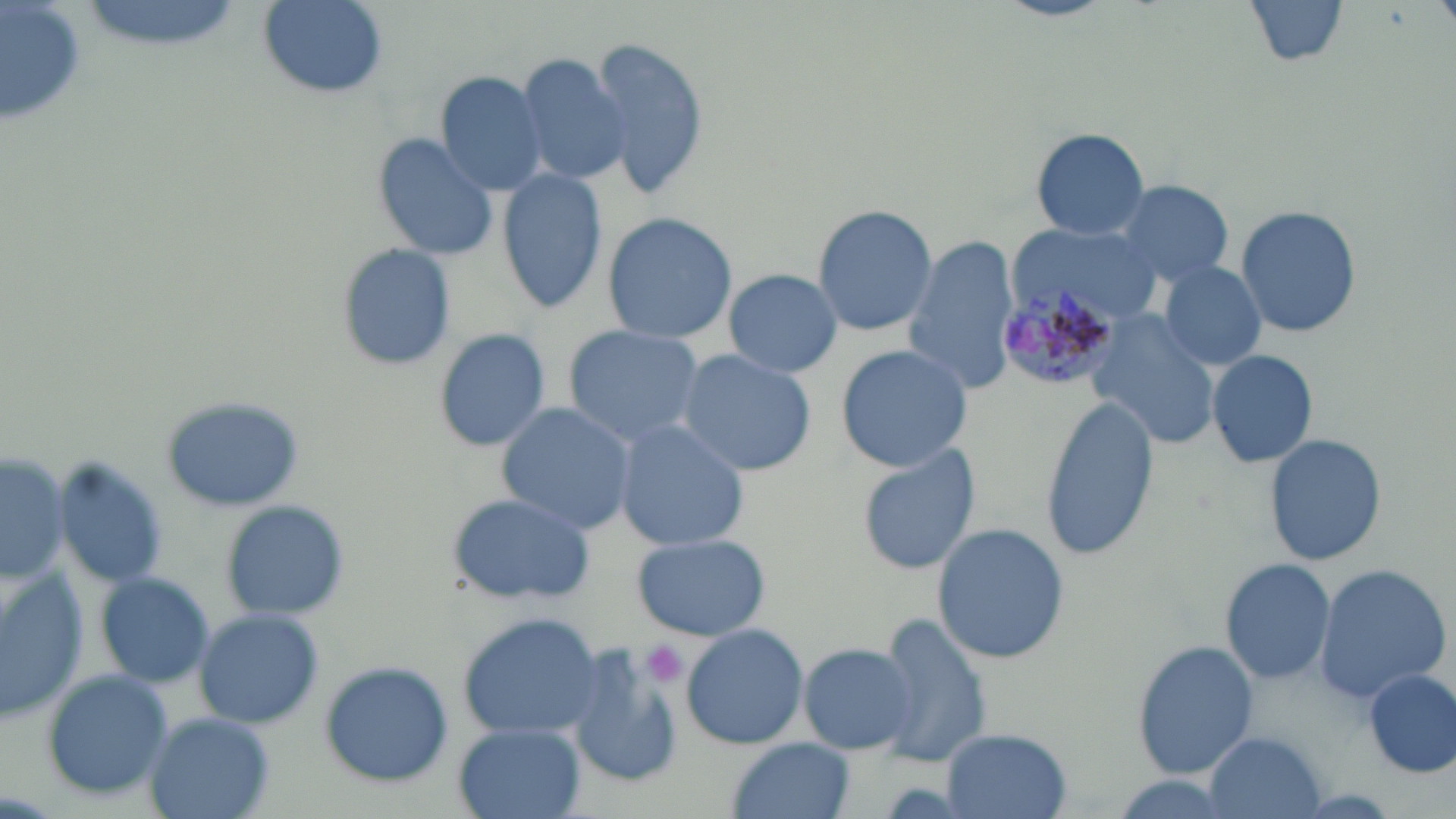
Approximate bounding boxes as (x1, y1, x2, y2) in pixels. Uninfected red blood cell locations: (257, 0, 390, 100), (997, 0, 1115, 22), (1243, 0, 1354, 71), (585, 32, 710, 200), (512, 52, 630, 185), (434, 70, 551, 197), (1028, 128, 1149, 241), (370, 131, 500, 264), (496, 166, 609, 314), (1108, 179, 1237, 285), (810, 203, 937, 336), (1236, 204, 1362, 340), (600, 211, 738, 345), (1012, 222, 1165, 327), (903, 236, 1020, 397), (334, 242, 456, 373), (1158, 260, 1269, 373), (723, 269, 843, 378), (1083, 314, 1221, 450), (561, 324, 703, 446), (432, 327, 556, 453), (834, 344, 972, 471), (677, 349, 815, 476), (1206, 349, 1319, 468), (159, 397, 302, 514), (1039, 397, 1161, 560), (496, 402, 637, 534), (613, 420, 750, 553), (1263, 432, 1388, 568), (856, 441, 983, 576), (0, 449, 70, 589), (49, 458, 172, 590), (443, 491, 596, 605), (219, 500, 349, 623), (933, 524, 1068, 666), (630, 532, 769, 641), (1220, 558, 1337, 687), (1311, 562, 1452, 705), (0, 569, 88, 720), (93, 569, 216, 688), (192, 608, 326, 730), (457, 613, 605, 740), (873, 615, 993, 769), (680, 623, 808, 750), (1130, 639, 1259, 782), (799, 644, 917, 754), (567, 648, 683, 789), (320, 661, 455, 788), (39, 668, 174, 800), (1363, 668, 1455, 778), (145, 712, 276, 819), (452, 723, 586, 819), (942, 728, 1072, 818), (1205, 731, 1327, 819), (727, 738, 856, 819). Platelet locations: (645, 641, 686, 687). Plasmodium malariae-infected red blood cell locations: (1001, 283, 1120, 389). Slide-level diagnosis: Plasmodium malariae. 1000x magnification. Thin blood film. Image is 1456×819 pixels. Single field of view. May-Grünwald-Giemsa-stained preparation. Light microscopy.